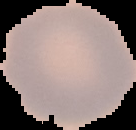
{
  "image_size": "136×130 pixels",
  "malaria_status": "uninfected",
  "image_type": "segmented cell region on a black background",
  "preparation": "thin blood film"
}